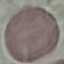

Summary:
  - Malaria status: uninfected
  - Preparation: thin blood smear
  - Stain: Giemsa
  - Capture: smartphone through the microscope eyepiece
  - Image type: automatically extracted cell patch, resized to 64 × 64 pixels